Report the malaria status of this cell.
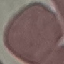
Uninfected.

Thin smear of blood. Giemsa stain. Automatically extracted cell patch, resized to 64 × 64 pixels. Photographed with a smartphone camera at the microscope eyepiece.